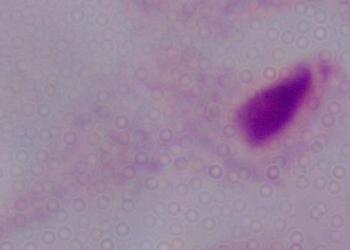

Summary:
  - Identification: trichomonad
  - Magnification: 1000x
  - Modality: micrograph